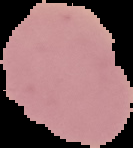

Summary:
  - Preparation: thin blood film
  - Image type: cell region segmented out of the field of view; surrounding area masked to black
  - Image size: 133×148 pixels
  - Result: no Plasmodium parasites detected